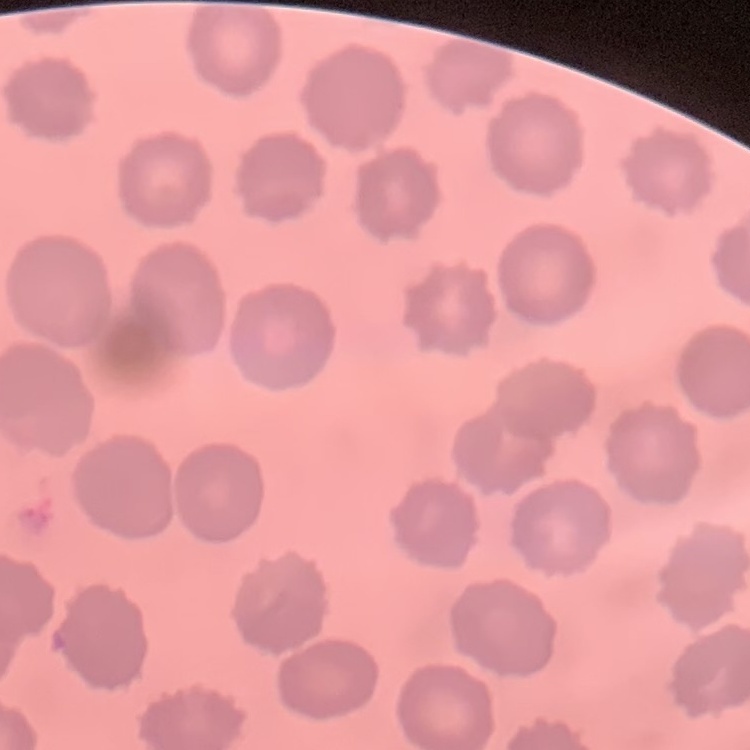 The erythrocytes show no rouleaux formation. Thin blood smear. Square crop of a larger photomicrograph. Field's or Giemsa stain.